Outline platelets.
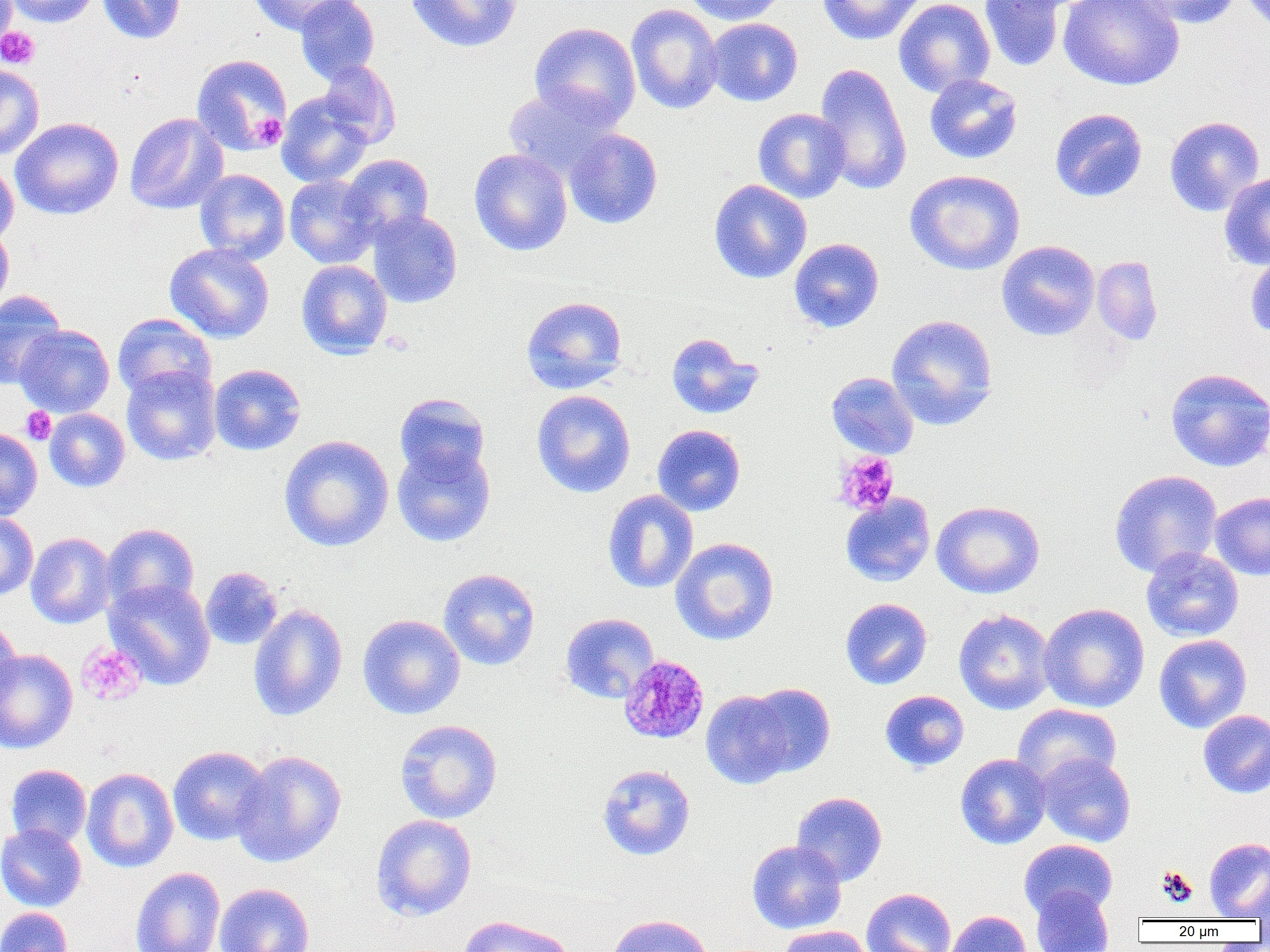
Approximate bounding boxes as (x1,y1)-(x2,y2) corner pairs in pixels.
Platelets: (0,26)-(40,69), (250,113)-(287,149), (21,407)-(56,444), (834,451)-(899,517), (76,641)-(147,706), (1156,866)-(1198,906).

{
  "slide_level_diagnosis": "Plasmodium malariae",
  "uninfected_red_blood_cell_locations": "approximate bounding boxes as (x1,y1)-(x2,y2) corner pairs in pixels: (0,0)-(17,51), (7,0)-(100,27), (96,0)-(185,44), (247,0)-(353,36), (295,0)-(380,83), (406,0)-(522,52), (681,0)-(788,25), (816,0)-(927,46), (894,0)-(995,97), (1058,0)-(1185,90), (1126,0)-(1243,28), (979,1)-(1066,72), (626,3)-(724,114), (704,18)-(803,107), (528,22)-(641,129), (191,53)-(292,155), (315,60)-(401,148), (813,62)-(912,195), (0,65)-(44,160), (924,74)-(1023,164), (503,86)-(623,183), (276,92)-(374,188), (753,108)-(851,203), (1050,108)-(1148,202), (124,113)-(228,215), (1164,116)-(1265,217), (10,117)-(124,220), (563,129)-(663,229), (469,148)-(572,256), (341,154)-(434,243), (0,162)-(19,247), (194,169)-(290,263), (904,169)-(1025,275), (1219,172)-(1270,270), (284,174)-(379,268), (709,179)-(811,283), (368,209)-(463,308), (0,223)-(14,314), (789,238)-(884,333), (996,240)-(1100,341), (164,242)-(275,343), (1245,251)-(1270,341), (1091,256)-(1163,345), (296,259)-(392,359), (0,290)-(67,389), (520,296)-(628,394), (112,313)-(216,403), (886,314)-(999,431), (14,324)-(115,418), (666,332)-(763,419), (209,364)-(306,455), (122,365)-(221,466), (1165,367)-(1270,472), (825,371)-(919,459), (531,389)-(636,498), (394,393)-(490,482), (45,408)-(130,492), (652,424)-(746,516), (0,427)-(42,520), (278,435)-(394,552), (392,443)-(496,547), (1109,469)-(1223,578), (602,489)-(699,594), (1210,491)-(1270,581), (840,493)-(935,586), (931,499)-(1045,599), (0,512)-(38,600), (101,523)-(199,613), (26,532)-(116,629), (670,537)-(779,645), (1140,547)-(1244,642), (200,566)-(283,650), (438,568)-(540,670), (104,578)-(216,690), (839,598)-(932,690), (1039,603)-(1150,712), (248,604)-(348,721), (954,608)-(1056,715), (560,612)-(659,703), (358,614)-(465,720), (0,618)-(22,712), (1154,634)-(1252,733), (0,649)-(78,753), (743,683)-(836,777), (701,690)-(797,789), (880,690)-(969,772), (1013,703)-(1122,789), (1197,709)-(1270,798), (394,719)-(503,823), (168,746)-(271,846), (233,749)-(347,867), (955,753)-(1051,849), (1036,753)-(1136,847), (82,760)-(270,859), (5,764)-(92,849), (597,764)-(696,861), (82,767)-(178,872), (791,791)-(888,886), (371,814)-(477,921), (0,823)-(87,911), (1204,837)-(1270,920), (1019,839)-(1118,920), (746,840)-(847,934), (130,867)-(226,952), (1251,881)-(1269,929), (215,883)-(314,952), (1030,887)-(1115,952), (861,888)-(957,952), (0,907)-(73,952), (946,910)-(1032,952), (605,913)-(714,952), (456,914)-(577,952), (778,926)-(872,952)",
  "field_of_view": "one of a larger specimen",
  "magnification": "1000x",
  "modality": "light microscopy",
  "image_size": "1270×952 pixels",
  "preparation": "thin blood film",
  "plasmodium_malariae_infected_red_blood_cell_locations": "approximate bounding boxes as (x1,y1)-(x2,y2) corner pairs in pixels: (618,655)-(710,744)"
}